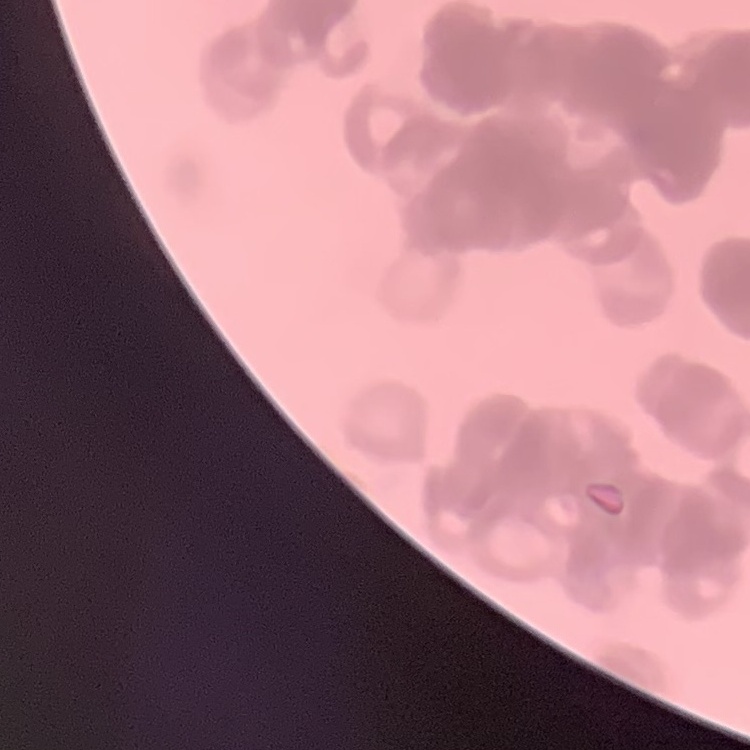
Summary:
  - Red blood cell morphology: rouleaux formation
  - Image type: one tile cut from a larger photomicrograph
  - Preparation: thin peripheral smear
  - Stain: Field's or Giemsa